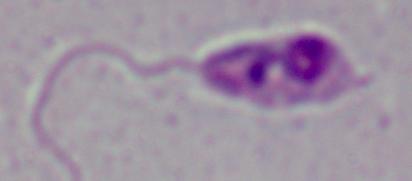

Micrograph. 1000x magnification. A Leishmania parasite is shown.